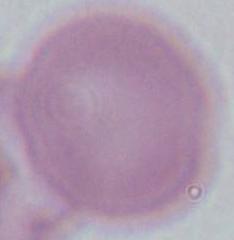
Summary:
  - Identification: erythrocyte
  - Magnification: 1000x
  - Modality: micrograph